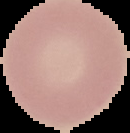

Summary:
  - Image type: cell region segmented out of the field of view; surrounding area masked to black
  - Malaria status: uninfected
  - Image size: 130×133 pixels
  - Preparation: thin blood film